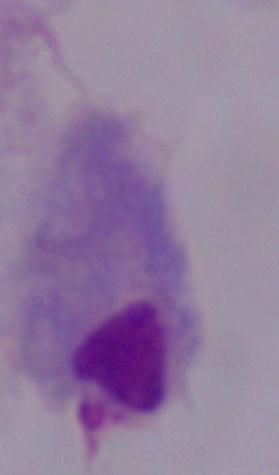
A trichomonad is shown. Micrograph. 1000x magnification.